Draw a bounding box around every parasitised red blood cell.
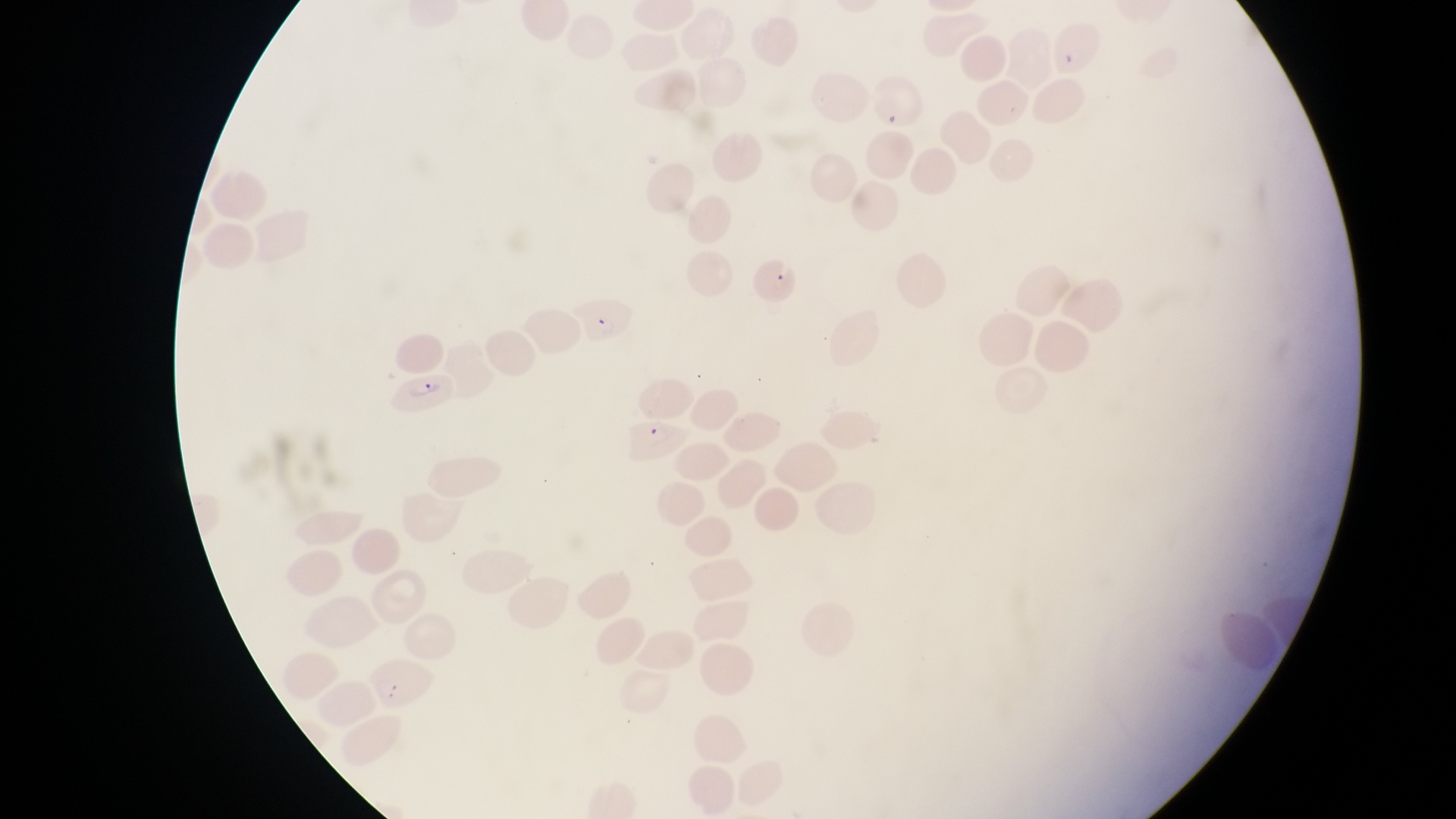

Approximate bounding boxes as left top right bottom in pixels.
Parasitised red blood cells: 871 72 924 136; 748 251 803 312; 576 297 634 355; 400 367 458 416.

Thin blood film. Sample from Uganda. Single field of view. Magnification of 1000x. Image is 1456×819 pixels. Captured by a smartphone held over the eyepiece of an Olympus CX-23 microscope.